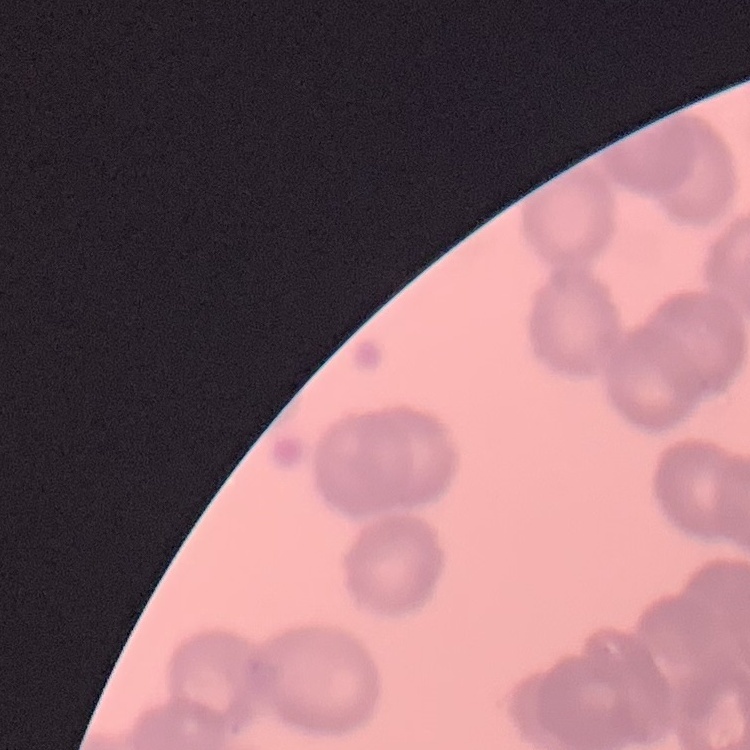

The red blood cells exhibit rouleaux formation. Field's or Giemsa stain. Thin blood film. Square crop of a larger photomicrograph.